Assess this cell for malaria.
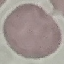

It is uninfected.

Acquired by smartphone through the microscope eyepiece. Thin blood film. Automatically extracted cell patch, resized to 64 × 64 pixels. Giemsa-stained preparation.